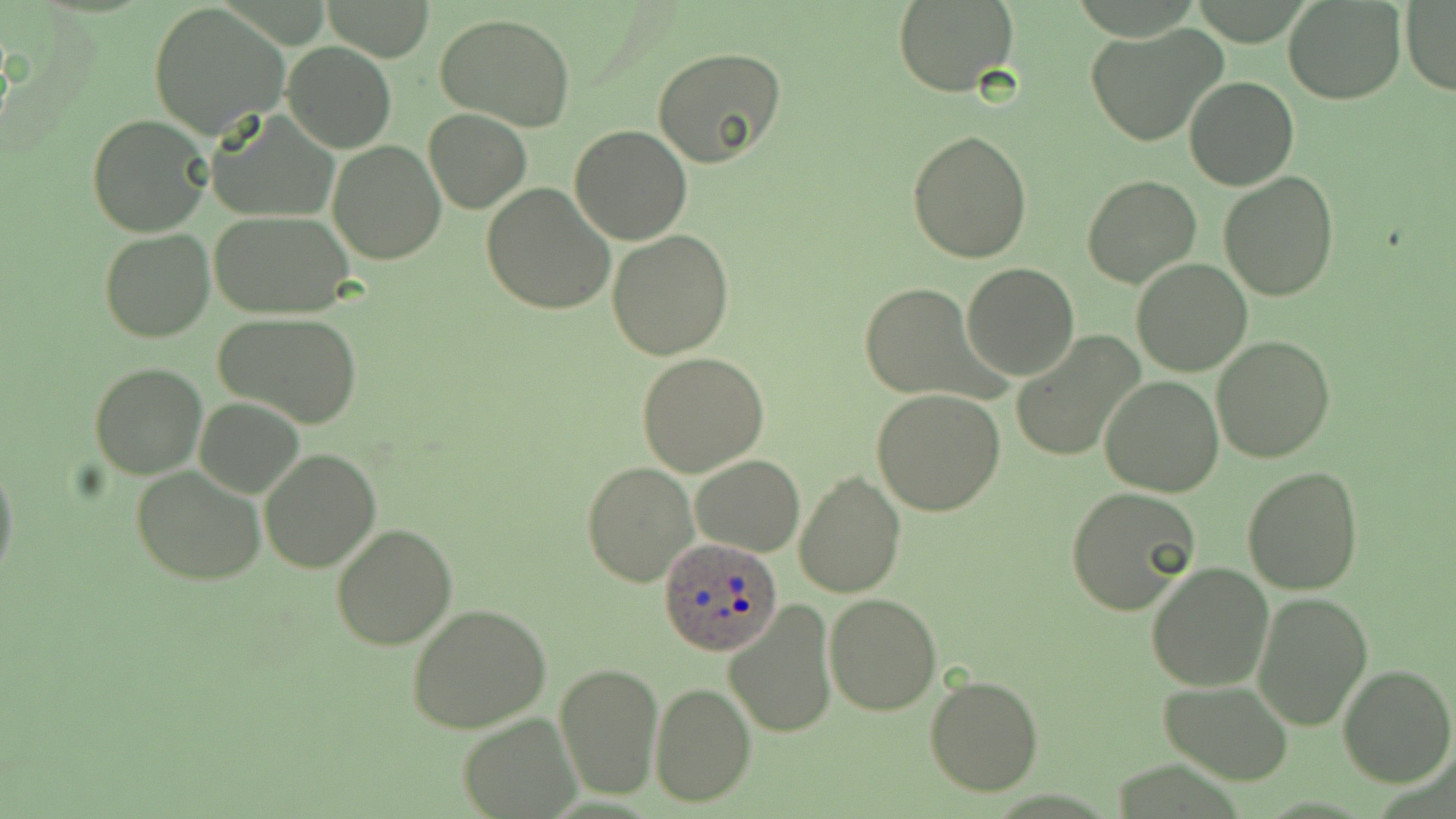
{
  "slide_level_diagnosis": "Plasmodium ovale",
  "preparation": "thin blood smear",
  "image_size": "1456×819 pixels",
  "plasmodium_ovale_infected_red_blood_cell_locations": "approximate bounding boxes as (x1,y1)-(x2,y2) corner pairs in pixels: (659,538)-(783,657)",
  "uninfected_red_blood_cell_locations": "approximate bounding boxes as (x1,y1)-(x2,y2) corner pairs in pixels: (322,0)-(435,62), (1283,0)-(1405,103), (892,1)-(1021,96), (1400,1)-(1456,98), (149,3)-(291,141), (434,14)-(577,130), (1085,25)-(1227,148), (282,40)-(396,153), (652,46)-(787,167), (1184,76)-(1298,190), (424,109)-(531,213), (207,111)-(336,223), (85,115)-(213,238), (571,124)-(692,245), (906,129)-(1034,264), (327,140)-(448,265), (1218,172)-(1340,302), (1082,175)-(1201,288), (481,182)-(616,316), (207,211)-(357,316), (98,230)-(215,343), (606,230)-(734,359), (1131,256)-(1252,375), (961,263)-(1079,380), (858,282)-(985,399), (213,313)-(363,428), (1010,331)-(1147,463), (1211,336)-(1336,463), (637,353)-(770,477), (90,362)-(207,479), (1099,375)-(1222,497), (871,390)-(1006,516), (193,398)-(305,497), (258,447)-(382,573), (690,454)-(804,556), (0,457)-(19,590), (582,461)-(699,588), (132,466)-(265,585), (1243,466)-(1363,594), (794,470)-(905,595), (1066,486)-(1200,615), (330,522)-(457,651), (1146,561)-(1275,692), (1250,591)-(1373,731), (824,594)-(940,715), (722,600)-(837,738), (408,604)-(553,735), (555,661)-(663,801), (1338,664)-(1455,786), (923,674)-(1043,799), (1159,680)-(1294,784), (650,683)-(755,805), (457,711)-(579,818)",
  "magnification": "1000x",
  "field_of_view": "single",
  "stain": "May-Grünwald-Giemsa",
  "modality": "optical microscopy"
}